Assess the morphology of the red blood cells.
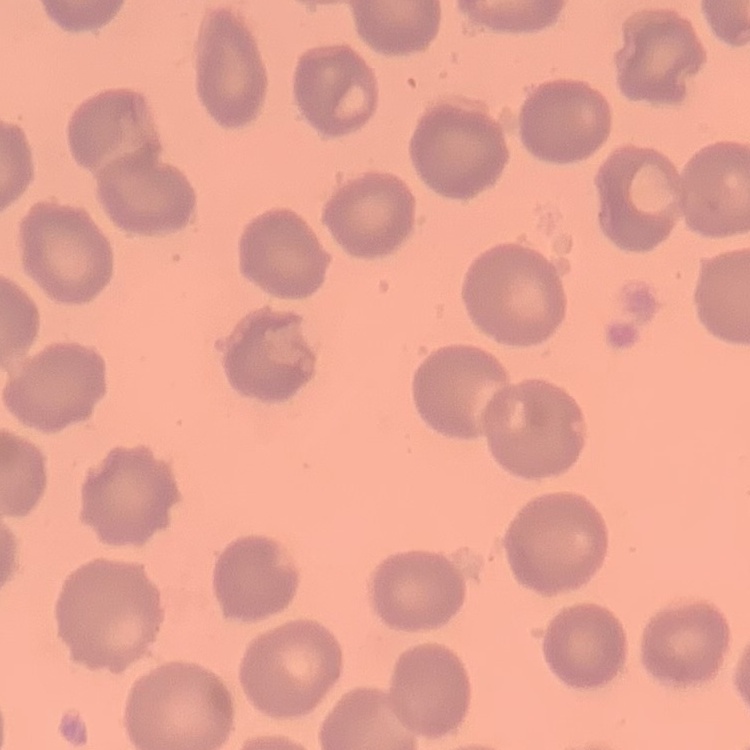

They show no rouleaux formation.

One tile cut from a larger photomicrograph. Thin blood film. Stained with either Field's or Giemsa.